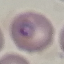

Result: malaria parasites identified. Photographed with a smartphone camera at the microscope eyepiece. Giemsa-stained preparation. Thin blood film. Cell patch, automatically extracted from a larger field of view and resized to 64 × 64 pixels.